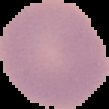

From a thin blood film. Image is 109×109 pixels. The area outside the segmented cell region is set to black. Result: no Plasmodium parasites seen.